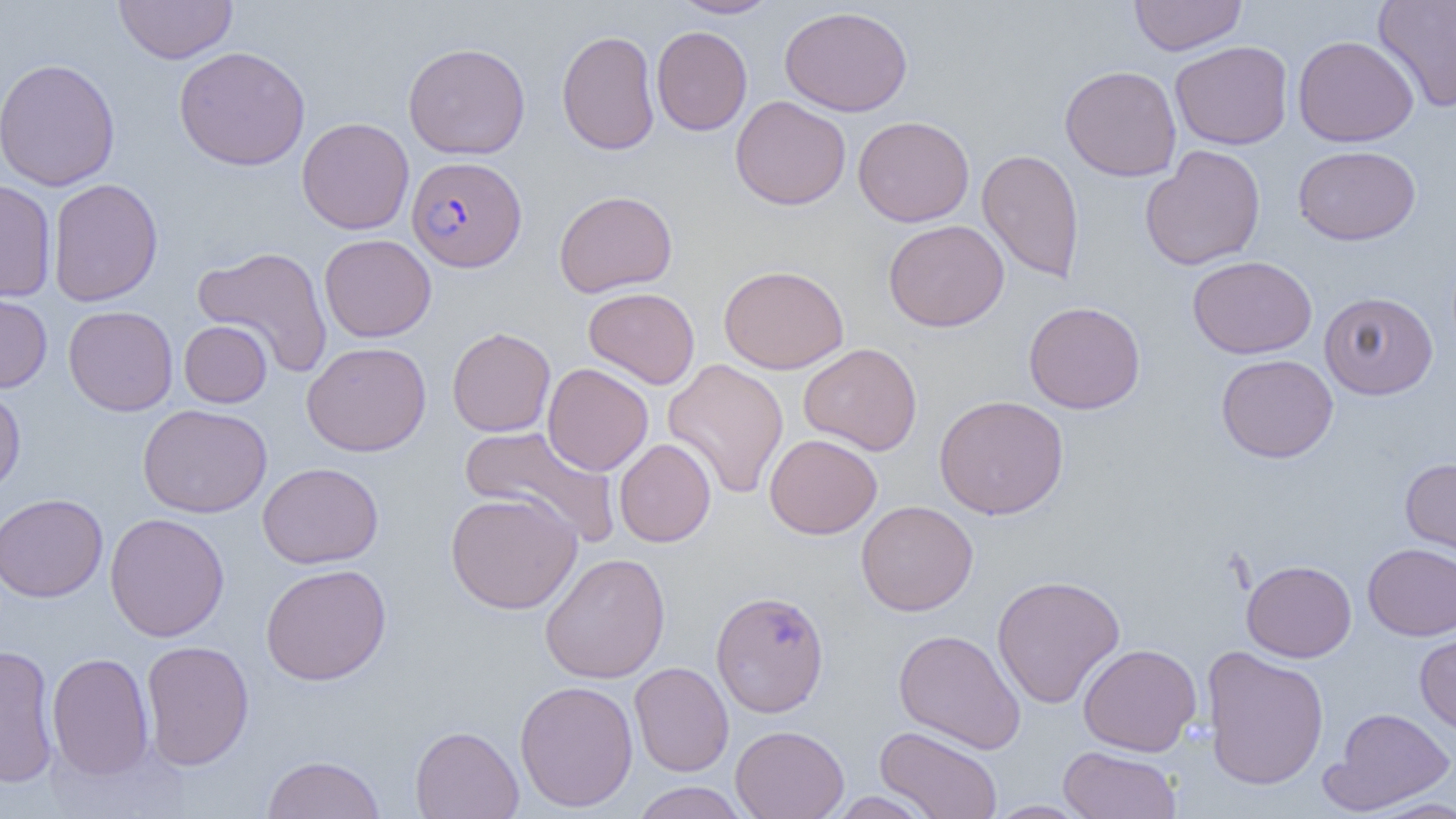

slide_level_diagnosis: Plasmodium falciparum
field_of_view: one of a larger specimen
magnification: 1000x
image_size: 1456×819 pixels
plasmodium_falciparum_infected_red_blood_cell_locations: 'approximate bounding boxes as (x1, y1, x2, y2) in pixels: (407, 156, 527, 272)'
preparation: thin blood smear
modality: light microscopy
uninfected_red_blood_cell_locations: 'approximate bounding boxes as (x1, y1, x2, y2) in pixels: (115, 0, 236, 64), (670, 0, 779, 19), (1129, 0, 1247, 56), (1373, 0, 1455, 112), (779, 5, 913, 116), (651, 26, 752, 136), (557, 29, 660, 156), (1292, 34, 1419, 147), (1170, 40, 1294, 150), (403, 42, 530, 159), (173, 46, 311, 170), (0, 58, 120, 191), (1059, 65, 1182, 181), (730, 96, 851, 210), (852, 115, 974, 227), (296, 117, 414, 235), (1140, 145, 1266, 271), (1293, 145, 1421, 245), (977, 149, 1085, 283), (47, 178, 163, 307), (0, 179, 57, 302), (553, 190, 678, 297), (883, 219, 1009, 332), (319, 234, 436, 342), (192, 245, 334, 377), (1187, 255, 1317, 359), (718, 264, 850, 374), (583, 287, 700, 389), (0, 288, 53, 394), (1319, 291, 1439, 399), (1023, 300, 1146, 414), (63, 305, 178, 416), (179, 320, 272, 408), (447, 327, 556, 437), (302, 341, 431, 456), (798, 342, 922, 455), (1216, 354, 1338, 463), (662, 358, 789, 500), (542, 362, 654, 476), (0, 384, 26, 499), (934, 394, 1069, 520), (137, 403, 272, 518), (458, 425, 621, 546), (764, 433, 882, 539), (614, 438, 716, 547), (1400, 457, 1456, 568), (257, 461, 383, 568), (445, 491, 582, 614), (0, 493, 108, 602), (856, 500, 978, 616), (105, 513, 229, 641), (1363, 543, 1456, 640), (539, 552, 671, 684), (1241, 559, 1357, 662), (260, 563, 391, 685), (991, 574, 1125, 708), (711, 589, 830, 718), (1414, 627, 1456, 738), (894, 629, 1026, 754), (140, 640, 254, 770), (1078, 643, 1202, 756), (0, 644, 59, 788), (1201, 646, 1329, 791), (47, 651, 154, 780), (629, 662, 734, 777), (514, 679, 639, 812), (1321, 707, 1456, 815), (410, 725, 523, 819), (731, 725, 849, 819), (875, 725, 1003, 819), (1058, 745, 1182, 818), (262, 754, 386, 819), (631, 781, 750, 819), (827, 791, 938, 818), (1362, 797, 1456, 818), (985, 800, 1093, 818)'